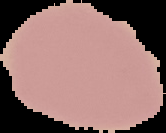
Image is 166×133 pixels. Cell region segmented out of the field of view; the surrounding area is masked to black. From a thin blood film. Malaria status: uninfected.